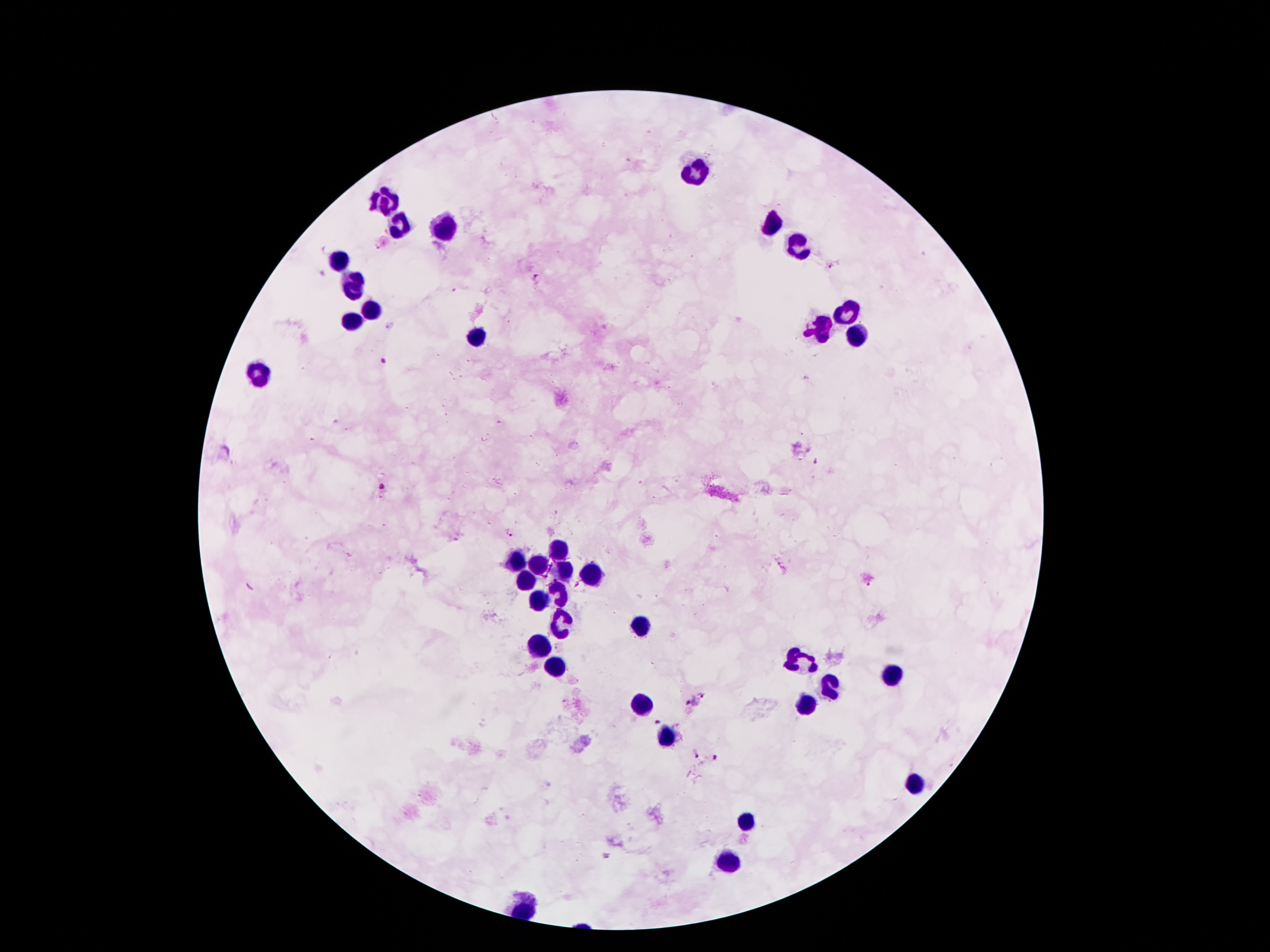
{
  "leukocyte_locations": "approximate centers as {x, y} in pixels: {695, 173}, {386, 200}, {400, 223}, {446, 225}, {775, 226}, {797, 245}, {339, 258}, {353, 287}, {371, 309}, {847, 314}, {355, 319}, {820, 330}, {858, 334}, {479, 339}, {257, 378}, {559, 550}, {520, 560}, {539, 562}, {564, 571}, {589, 574}, {525, 583}, {559, 593}, {538, 600}, {561, 622}, {640, 627}, {539, 643}, {802, 662}, {555, 668}, {892, 677}, {829, 684}, {643, 703}, {806, 707}, {666, 734}, {913, 784}, {747, 824}, {729, 862}",
  "patient_malaria_status": "infected with Plasmodium falciparum",
  "stain": "Giemsa",
  "field_of_view": "one from this slide",
  "capture": "smartphone camera through the microscope eyepiece",
  "malaria_parasite_locations": "approximate centers as {x, y} in pixels: {830, 267}, {538, 278}, {818, 461}, {509, 534}, {705, 693}, {688, 704}, {657, 722}, {694, 755}, {714, 757}, {607, 856}",
  "preparation": "thick blood film",
  "magnification": "100x",
  "image_size": "1270×952 pixels"
}